Report the malaria status of this cell.
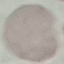
It is uninfected.

Giemsa stain. Thin blood smear. Automatically extracted cell patch, resized to 64 × 64 pixels. Photographed with a smartphone camera at the microscope eyepiece.